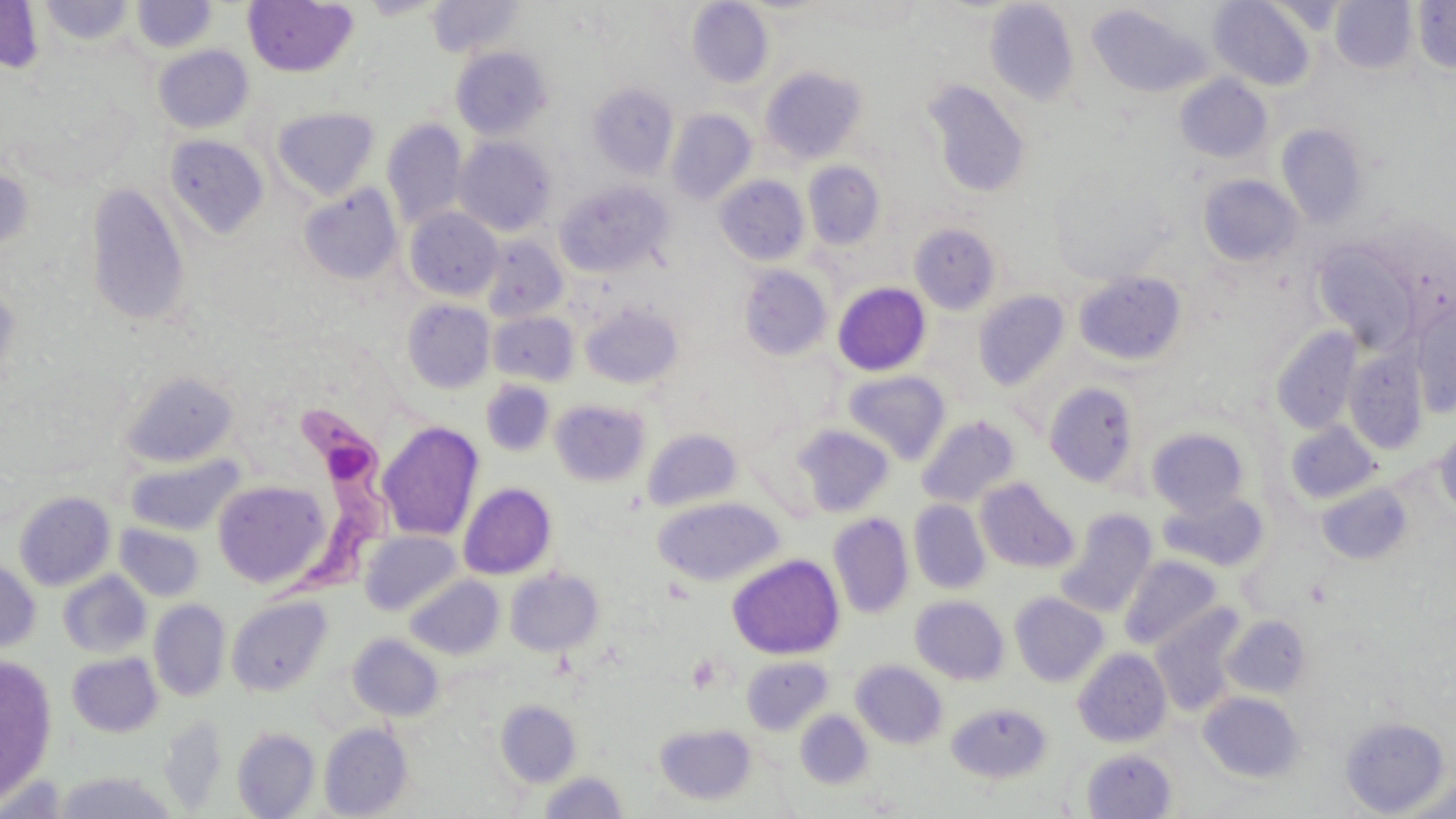
Summary:
  - Coordinate format: approximate bounding boxes as (x1,y1)-(x2,y2) corner pairs in pixels
  - Trypanosoma brucei locations: (268,397)-(394,616)
  - Uninfected red blood cell locations: (426,0)-(526,57), (1208,0)-(1316,91), (1330,0)-(1416,73), (0,1)-(44,75), (39,1)-(134,45), (131,1)-(217,54), (242,1)-(359,78), (687,1)-(774,88), (984,1)-(1079,106), (1412,1)-(1456,75), (1086,4)-(1210,99), (153,45)-(253,133), (451,46)-(552,139), (759,65)-(868,165), (1174,74)-(1272,163), (923,80)-(1031,199), (587,82)-(678,179), (272,106)-(379,199), (666,109)-(756,204), (382,119)-(468,230), (1276,122)-(1368,228), (163,134)-(269,239), (455,136)-(557,236), (802,161)-(885,250), (0,163)-(34,259), (1198,174)-(1302,267), (714,175)-(810,266), (556,181)-(672,277), (85,182)-(192,327), (299,183)-(402,285), (404,207)-(503,301), (909,223)-(1002,315), (479,236)-(568,323), (1311,239)-(1423,352), (737,264)-(833,362), (1074,271)-(1187,366), (0,282)-(22,392), (832,282)-(931,376), (973,290)-(1071,391), (402,299)-(495,393), (579,301)-(683,389), (1410,308)-(1456,417), (488,310)-(579,386), (1271,326)-(1362,435), (1343,350)-(1427,454), (121,370)-(241,469), (842,370)-(950,464), (480,379)-(556,457), (1043,382)-(1140,488), (550,398)-(651,487), (916,415)-(1020,508), (1285,420)-(1382,505), (377,422)-(484,541), (1434,424)-(1456,519), (791,425)-(894,517), (642,428)-(743,512), (1146,428)-(1250,518), (125,454)-(243,536), (975,477)-(1078,573), (212,479)-(330,589), (1317,481)-(1413,566), (458,482)-(557,580), (14,491)-(116,591), (1157,491)-(1269,572), (652,496)-(784,586), (909,500)-(990,594), (1056,508)-(1158,617), (827,512)-(914,619), (114,522)-(205,602), (360,531)-(462,615), (727,553)-(844,660), (1120,555)-(1222,649), (0,558)-(40,653), (505,568)-(604,656), (58,571)-(151,658), (405,575)-(504,660), (1009,592)-(1109,686), (227,596)-(332,697), (911,596)-(1009,684), (149,599)-(231,701), (1150,607)-(1243,715), (1223,615)-(1311,699), (348,633)-(444,721), (1073,647)-(1172,747), (67,652)-(163,737), (0,655)-(57,803), (742,656)-(833,734), (851,659)-(948,749), (1198,691)-(1305,782), (495,699)-(582,787), (947,702)-(1052,783), (795,710)-(873,789), (157,715)-(228,814), (1338,715)-(1452,815), (654,722)-(757,806), (319,723)-(413,818), (233,727)-(320,818), (1081,748)-(1177,818), (538,771)-(629,818), (52,772)-(180,818), (0,774)-(70,817)
  - Slide-level diagnosis: Trypanosoma brucei
  - Preparation: thin blood smear
  - Modality: optical microscopy
  - Field of view: one of a larger specimen
  - Stain: May-Grünwald-Giemsa
  - Image size: 1456×819 pixels
  - Magnification: 1000x